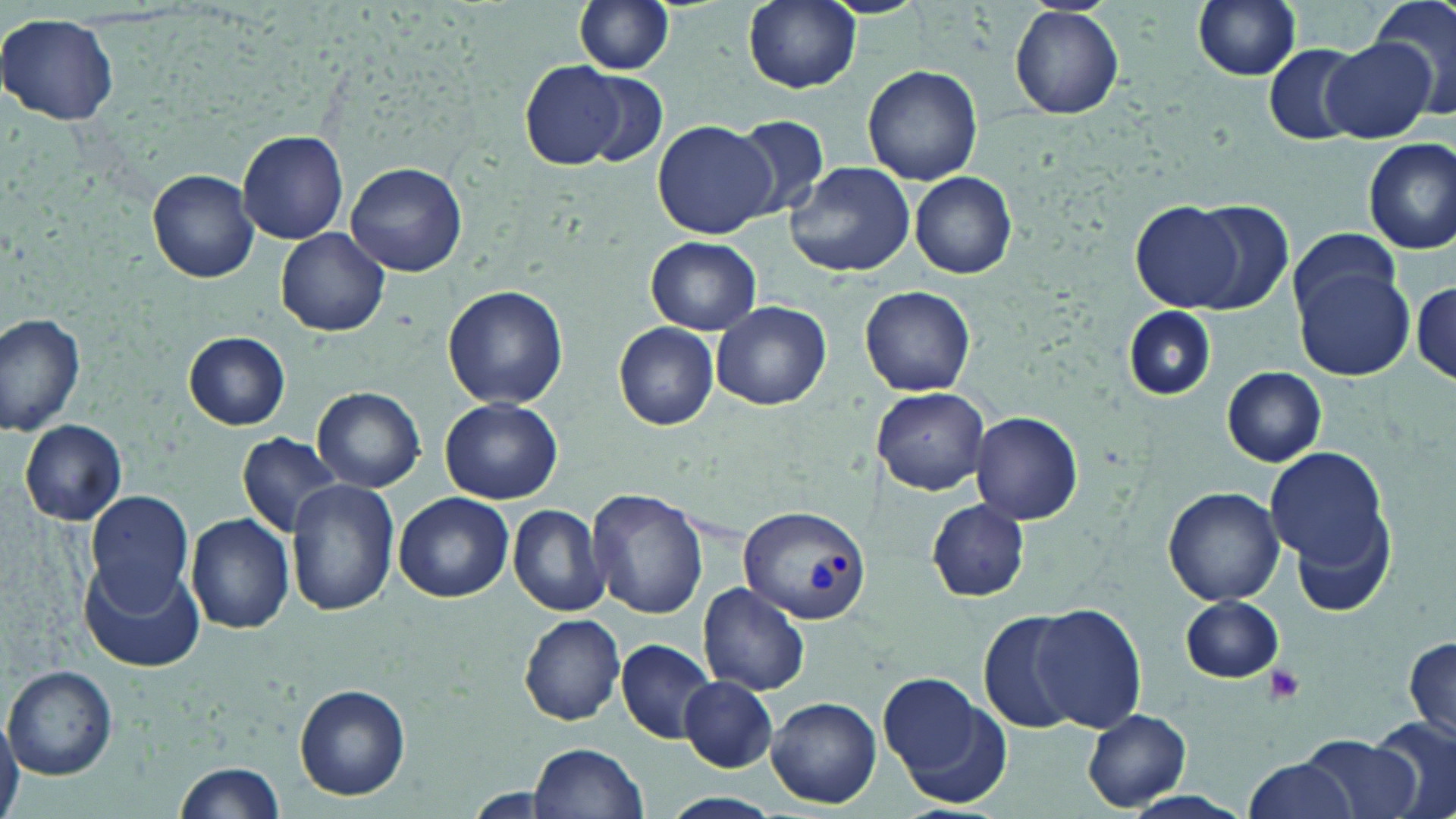
Approximate bounding boxes as [x1, y1, x2, y2] in pixels. Plasmodium vivax-infected red blood cell locations: [741, 507, 872, 624]. Uninfected red blood cell locations: [573, 0, 675, 75], [1192, 0, 1304, 81], [1371, 0, 1456, 114], [742, 1, 862, 94], [1010, 5, 1123, 119], [0, 14, 120, 126], [1323, 38, 1435, 142], [1265, 44, 1367, 144], [521, 63, 626, 170], [862, 64, 983, 186], [576, 68, 669, 168], [731, 113, 830, 222], [653, 119, 776, 239], [237, 131, 348, 244], [1362, 138, 1456, 256], [786, 160, 916, 278], [346, 162, 468, 277], [148, 170, 259, 283], [910, 172, 1018, 279], [1187, 199, 1295, 315], [1131, 201, 1247, 311], [277, 227, 390, 337], [1286, 228, 1407, 322], [645, 236, 762, 335], [1294, 264, 1414, 381], [1412, 280, 1455, 384], [444, 285, 567, 408], [860, 286, 976, 397], [710, 300, 831, 411], [1123, 308, 1213, 401], [0, 313, 85, 438], [613, 321, 719, 430], [184, 331, 290, 430], [1223, 367, 1326, 466], [313, 386, 425, 492], [871, 388, 990, 494], [440, 396, 562, 503], [970, 411, 1083, 525], [20, 420, 127, 526], [236, 433, 348, 538], [1265, 440, 1391, 589], [287, 478, 396, 617], [1164, 486, 1285, 604], [585, 488, 708, 620], [84, 490, 192, 611], [393, 492, 513, 604], [927, 500, 1030, 601], [508, 503, 612, 617], [187, 514, 296, 634], [79, 559, 205, 673], [700, 582, 811, 695], [1180, 596, 1286, 683], [1028, 604, 1147, 733], [980, 610, 1083, 734], [519, 613, 627, 726], [1403, 633, 1456, 748], [616, 638, 716, 743], [3, 665, 117, 780], [880, 675, 1009, 803], [678, 676, 777, 772], [295, 683, 412, 801], [767, 696, 882, 807], [1082, 709, 1192, 811], [1371, 720, 1455, 819], [0, 721, 22, 816], [1296, 734, 1422, 819], [529, 742, 647, 819], [1239, 757, 1360, 819], [173, 758, 289, 819], [661, 792, 786, 819]. Platelet locations: [1260, 665, 1307, 707]. Slide-level diagnosis: Plasmodium vivax. 1000x magnification. May-Grünwald-Giemsa-stained preparation. Single field of view. Optical microscopy. Image is 1456×819 pixels. Thin blood film.